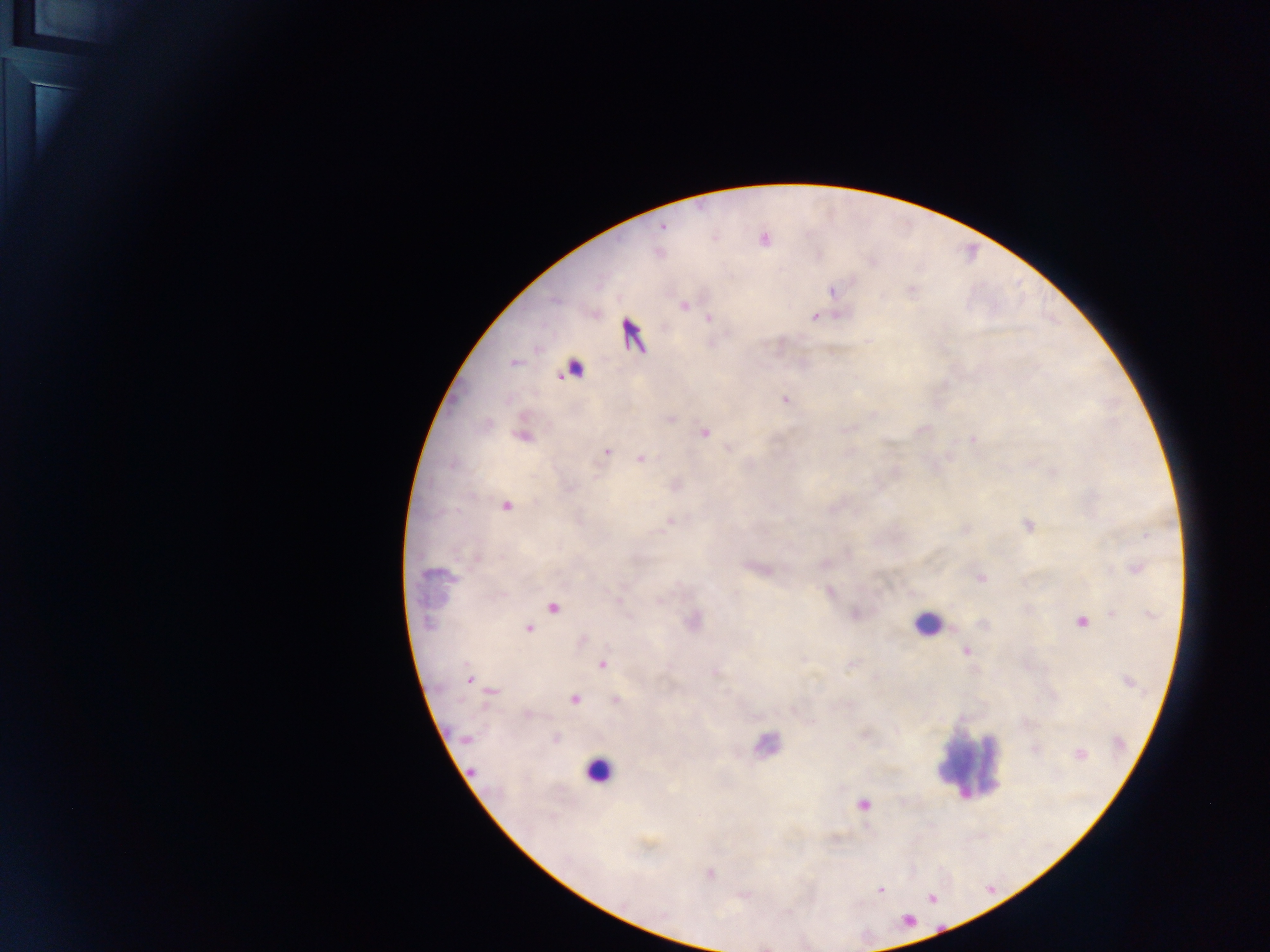

Approximate centers as [x, y] in pixels. Leukocyte locations: [926, 624], [763, 743], [967, 763], [597, 770]. Plasmodium parasite locations: [663, 228], [832, 291], [684, 306], [814, 317], [708, 318], [633, 336], [514, 362], [574, 369], [785, 400], [671, 419], [705, 433], [524, 437], [973, 439], [607, 452], [640, 458], [505, 507], [670, 520], [1028, 525], [1135, 568], [980, 578], [552, 607], [1112, 613], [1081, 622], [428, 623], [528, 628], [966, 651], [602, 664], [470, 680], [492, 691], [616, 699], [574, 700], [527, 714], [465, 739], [1080, 754], [471, 771], [863, 804], [710, 873], [880, 890]. Single field of view. Collected in Ghana. Thick blood smear. Image is 1270×952 pixels. Mobile-phone photograph taken through the microscope.